Outline each blood parasite and name the species.
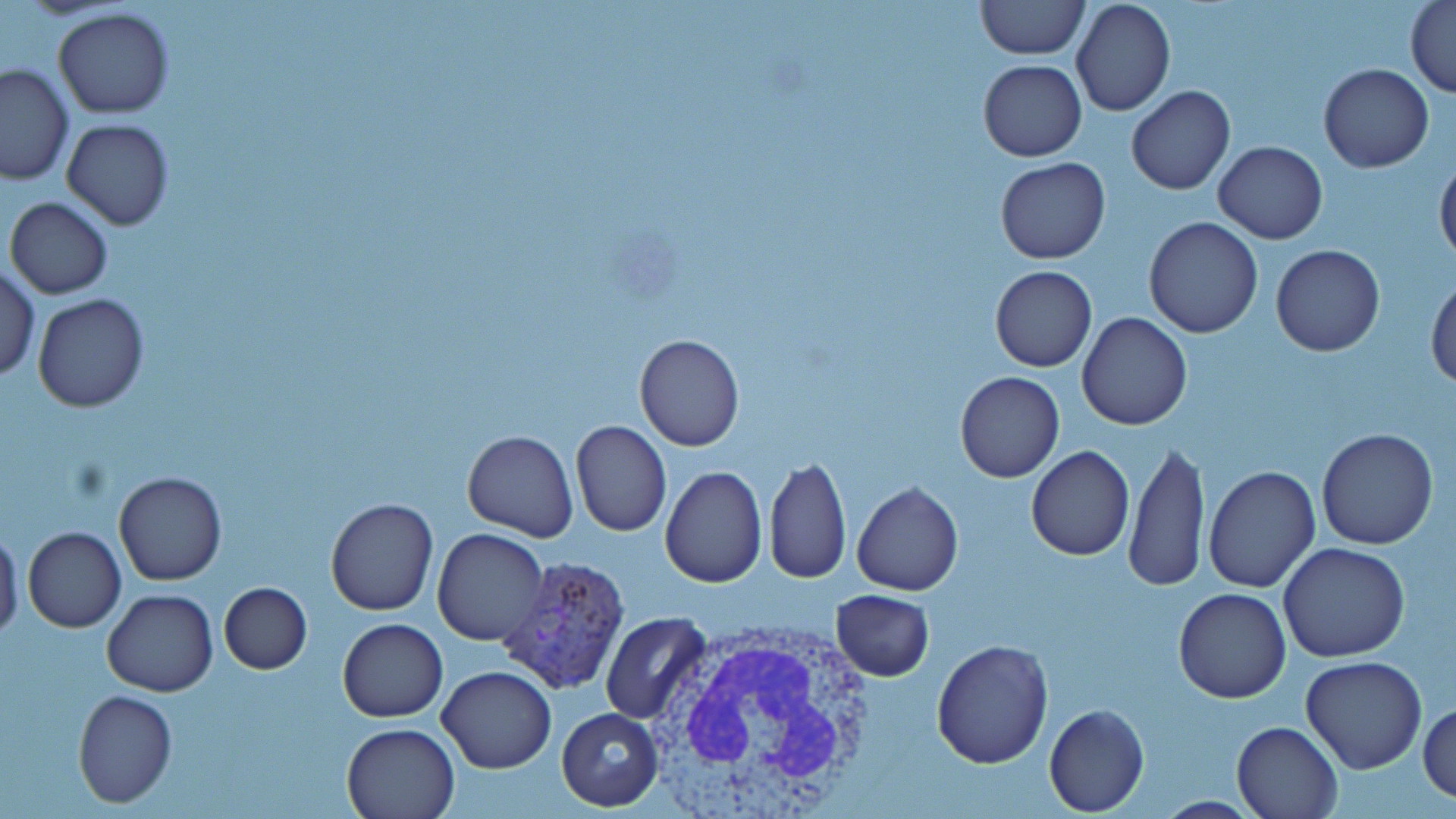
Approximate bounding boxes as (x1,y1)-(x2,y2) corner pairs in pixels.
Plasmodium vivax-infected red blood cells: (497,558)-(632,694).
No Plasmodium falciparum, Plasmodium ovale, Plasmodium malariae, Babesia divergens, or Trypanosoma brucei observed.

Uninfected red blood cell locations: (975,0)-(1088,61), (1404,0)-(1455,98), (1071,1)-(1175,118), (53,7)-(175,119), (978,60)-(1086,161), (1,63)-(76,185), (1319,63)-(1433,172), (1126,86)-(1234,194), (61,119)-(174,231), (1213,141)-(1327,244), (1435,156)-(1456,264), (995,158)-(1111,265), (4,196)-(113,300), (1143,217)-(1263,339), (1270,244)-(1384,355), (0,265)-(40,382), (989,265)-(1096,373), (1427,274)-(1456,390), (32,292)-(150,413), (1077,312)-(1192,430), (634,333)-(745,451), (954,371)-(1064,483), (569,419)-(672,537), (1316,426)-(1440,550), (461,430)-(579,542), (1125,438)-(1207,593), (1026,446)-(1134,562), (764,454)-(850,584), (660,464)-(767,587), (1202,464)-(1321,593), (113,470)-(227,585), (851,481)-(962,595), (326,497)-(438,615), (0,526)-(24,644), (23,527)-(126,632), (431,529)-(551,646), (1278,543)-(1410,663), (218,581)-(312,674), (1174,587)-(1291,703), (830,589)-(936,682), (101,590)-(218,695), (601,611)-(712,725), (338,618)-(448,722), (932,640)-(1054,769), (1301,656)-(1427,774), (436,666)-(556,775), (72,689)-(178,808), (1418,700)-(1456,804), (1043,703)-(1148,815), (557,708)-(665,811), (1232,719)-(1344,819), (340,723)-(461,818). White blood cell locations: (653,618)-(882,819). Slide-level diagnosis: Plasmodium vivax. Image is 1456×819 pixels. Thin blood smear. Light microscopy. One field of a larger specimen. 1000x magnification. May-Grünwald-Giemsa-stained preparation.